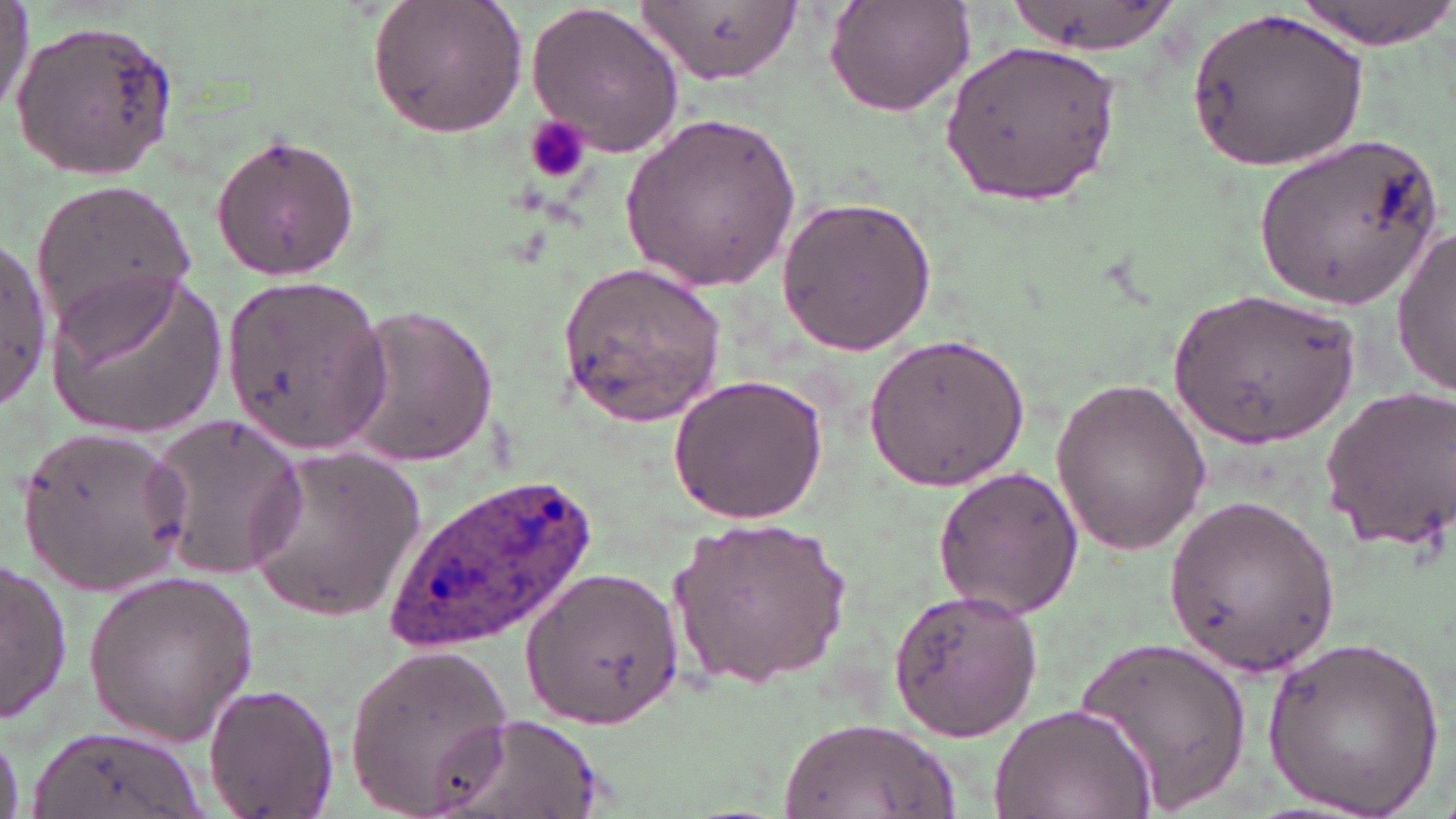

Summary:
  - Coordinate format: approximate bounding boxes as (x1, y1, x2, y2) in pixels
  - Uninfected red blood cell locations: (366, 0, 527, 138), (824, 0, 976, 118), (999, 0, 1179, 59), (1289, 0, 1453, 48), (0, 1, 34, 115), (638, 1, 803, 88), (525, 3, 684, 157), (1189, 7, 1369, 170), (7, 19, 181, 184), (942, 32, 1121, 210), (620, 111, 800, 294), (207, 132, 365, 281), (1253, 132, 1446, 313), (28, 175, 204, 340), (775, 195, 937, 356), (1391, 225, 1455, 397), (0, 237, 51, 408), (558, 261, 726, 426), (45, 273, 227, 438), (223, 274, 390, 453), (1170, 288, 1361, 449), (341, 305, 499, 469), (863, 331, 1032, 493), (666, 373, 830, 525), (1047, 376, 1212, 555), (1316, 382, 1456, 557), (144, 408, 309, 585), (18, 423, 191, 593), (244, 446, 426, 621), (933, 465, 1084, 621), (1163, 495, 1344, 675), (670, 515, 856, 687), (1, 556, 74, 725), (518, 566, 684, 731), (81, 570, 261, 743), (886, 584, 1040, 741), (1264, 630, 1443, 818), (1076, 633, 1252, 813), (343, 642, 516, 818), (202, 681, 339, 819), (991, 702, 1157, 819), (432, 711, 605, 819), (778, 718, 960, 817), (27, 725, 209, 819), (0, 732, 26, 815)
  - Platelet locations: (525, 114, 590, 185)
  - Plasmodium ovale-infected red blood cell locations: (380, 472, 606, 654)
  - Slide-level diagnosis: Plasmodium ovale
  - Field of view: one of a larger specimen
  - Magnification: 1000x
  - Image size: 1456×819 pixels
  - Preparation: thin blood smear
  - Modality: optical microscopy
  - Stain: May-Grünwald-Giemsa